Report the malaria status of this cell.
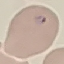
Parasitized.

Photographed with a smartphone camera at the microscope eyepiece. Cell patch, automatically extracted from a larger field of view and resized to 64 × 64 pixels. Thin blood film. Giemsa stain.